Report the malaria status of this cell.
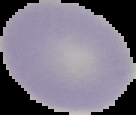

Uninfected.

Summary:
  - Image size: 136×115 pixels
  - Preparation: thin blood smear
  - Image type: segmented cell region on a black background